Locate every malaria parasite and every leukocyte.
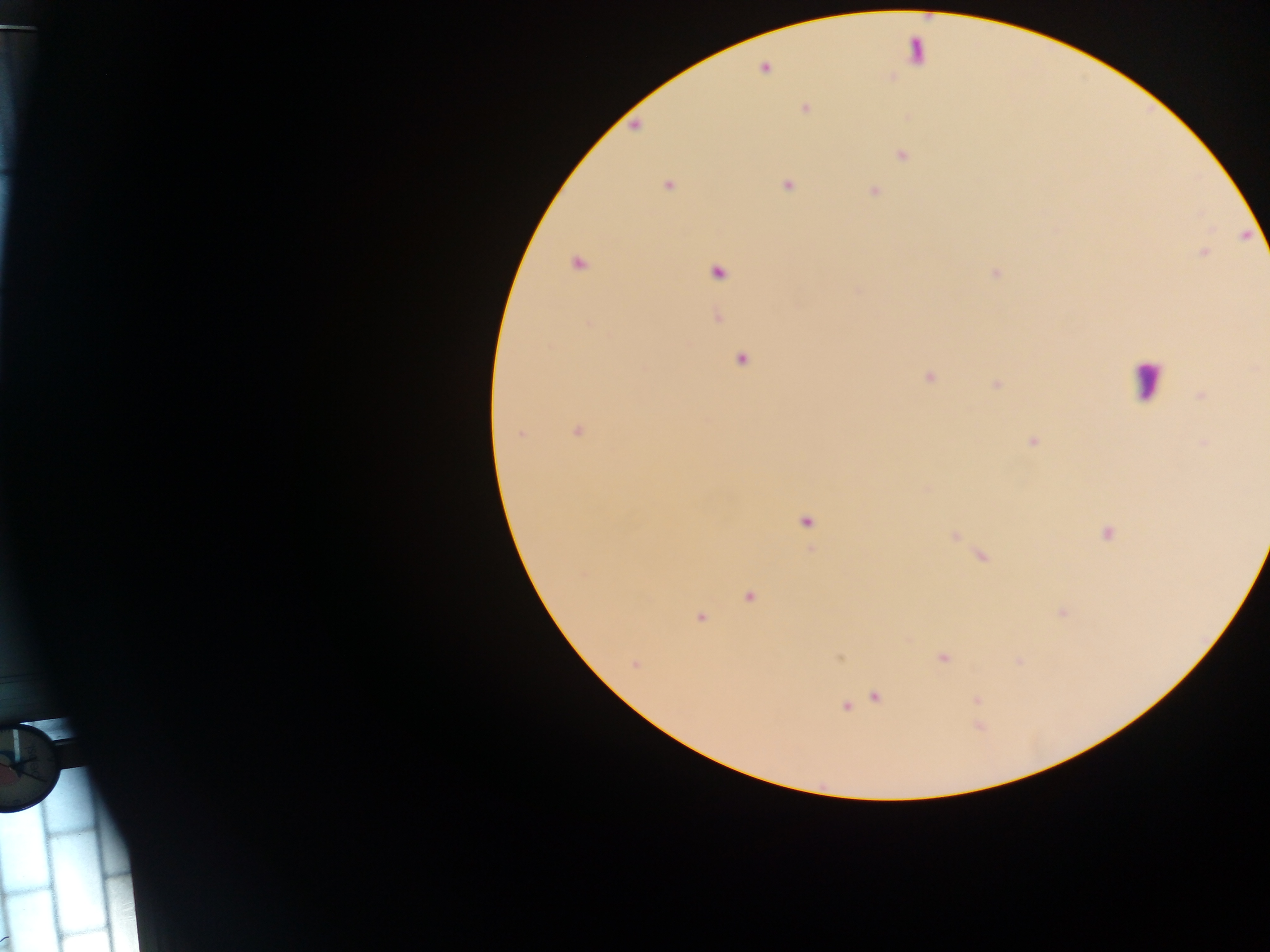
Approximate centers as x y in pixels.
Malaria parasites: 805 109; 902 155; 668 185; 788 185; 875 191; 577 264; 718 273; 995 274; 589 324; 741 360; 929 377; 996 384; 1202 396; 578 431; 520 434; 1032 442; 1203 443; 806 522; 1107 533; 955 537; 748 597; 1062 612; 700 618; 943 658; 635 664; 876 697; 978 699; 845 707; 7 936.
Leukocytes: 913 50; 1145 381.

Summary:
  - Capture: mobile-phone photograph through a microscope
  - Field of view: single
  - Country: Ghana
  - Preparation: thick blood film
  - Image size: 1270×952 pixels